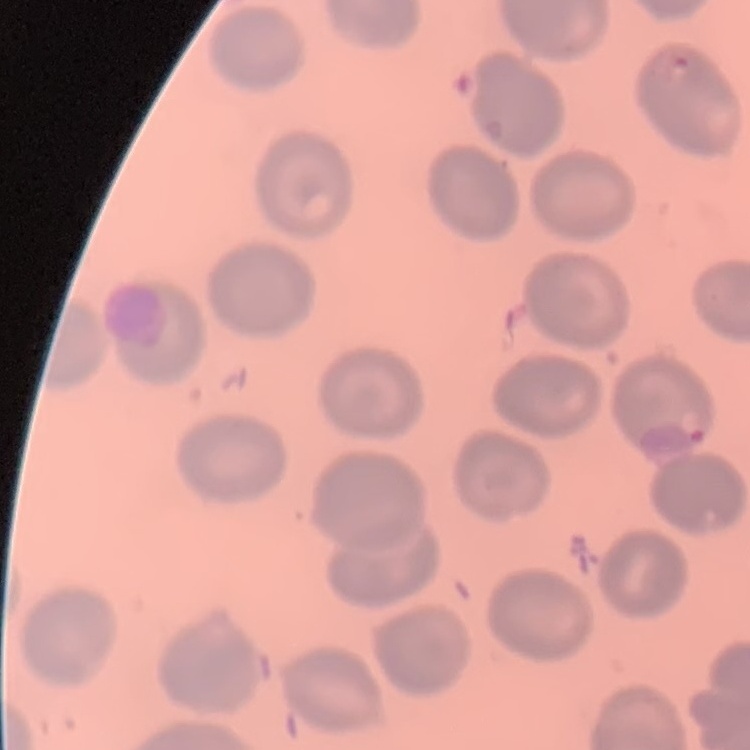

The erythrocytes exhibit no rouleaux formation. Thin peripheral smear. One tile cut from a larger photomicrograph. Stained with either Field's or Giemsa.